Describe the morphology of the red blood cells.
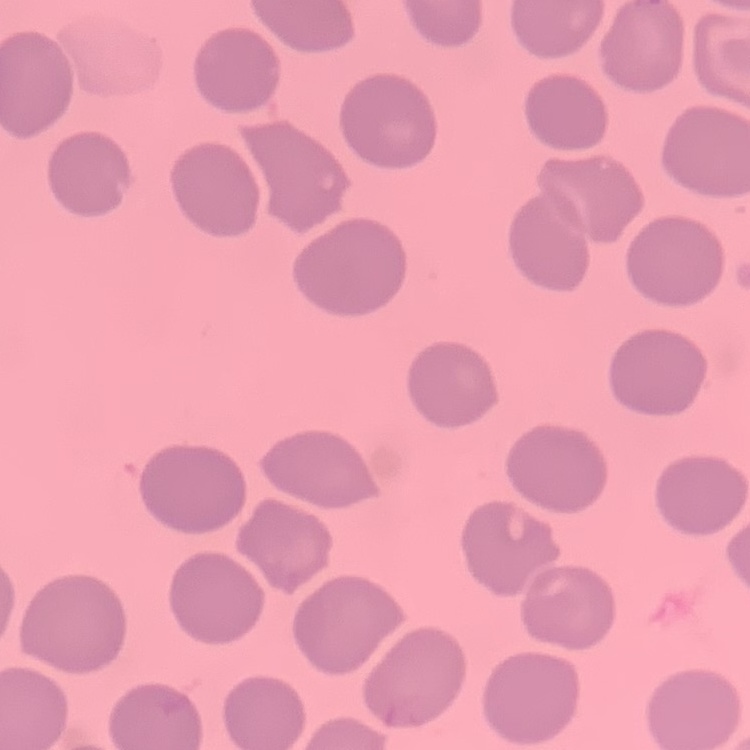

No rouleaux formation.

Summary:
  - Image type: one tile cut from a larger photomicrograph
  - Preparation: thin blood smear
  - Stain: Field's or Giemsa